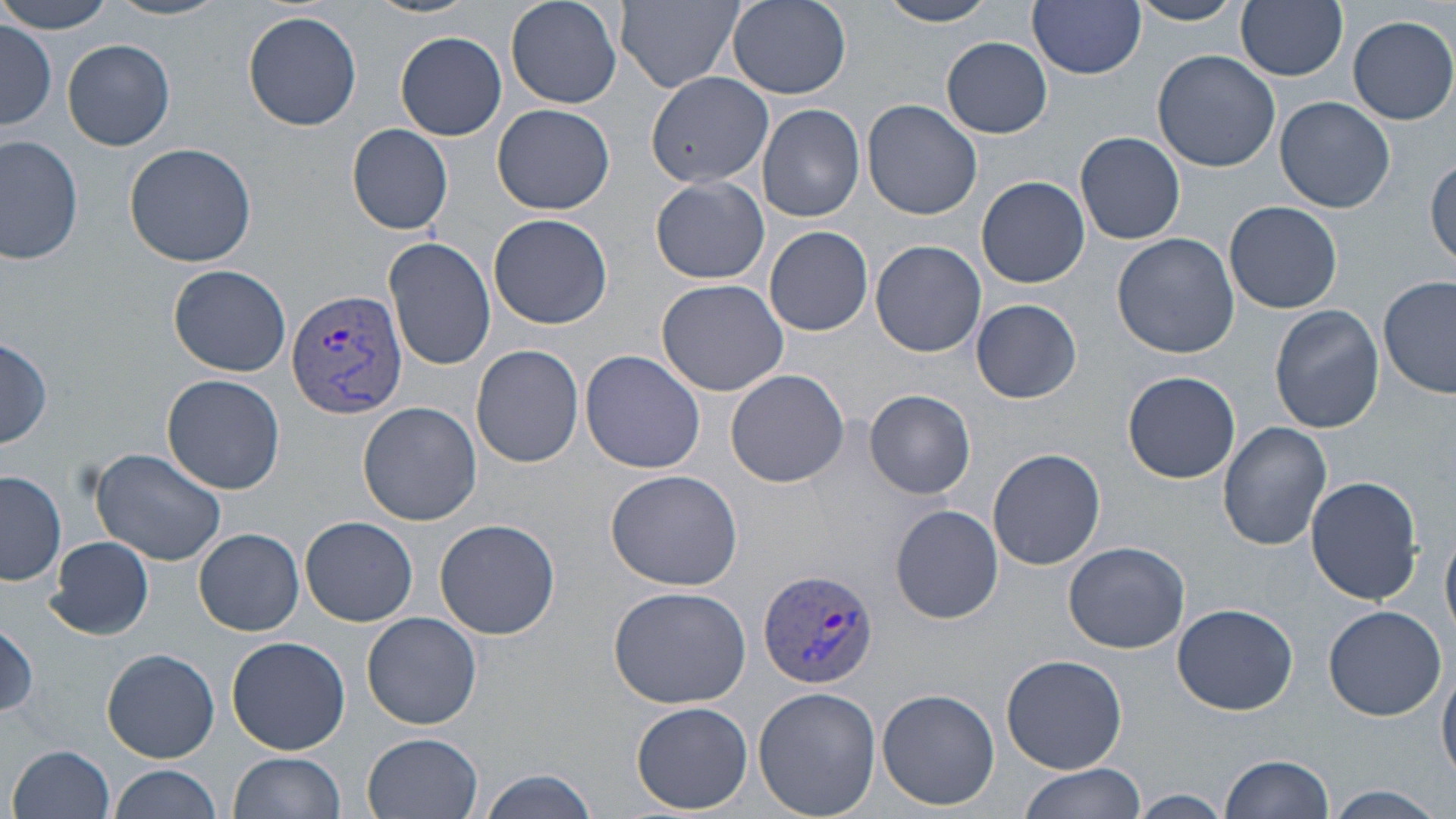

Approximate bounding boxes as named x1/y1/x2/y2 corners in pixels. Uninfected red blood cell locations: (x1=2, y1=0, x2=117, y2=34), (x1=107, y1=0, x2=231, y2=21), (x1=364, y1=0, x2=483, y2=19), (x1=506, y1=0, x2=623, y2=108), (x1=727, y1=0, x2=852, y2=98), (x1=878, y1=0, x2=999, y2=26), (x1=1129, y1=0, x2=1244, y2=25), (x1=1237, y1=0, x2=1348, y2=81), (x1=616, y1=1, x2=745, y2=93), (x1=1028, y1=1, x2=1145, y2=79), (x1=244, y1=11, x2=363, y2=131), (x1=1348, y1=14, x2=1456, y2=124), (x1=1, y1=24, x2=55, y2=130), (x1=395, y1=31, x2=506, y2=141), (x1=941, y1=38, x2=1052, y2=138), (x1=63, y1=39, x2=175, y2=151), (x1=1151, y1=48, x2=1279, y2=174), (x1=644, y1=70, x2=773, y2=191), (x1=1275, y1=96, x2=1397, y2=214), (x1=863, y1=101, x2=983, y2=220), (x1=492, y1=103, x2=615, y2=215), (x1=757, y1=104, x2=865, y2=222), (x1=345, y1=124, x2=455, y2=235), (x1=1074, y1=132, x2=1185, y2=245), (x1=1, y1=135, x2=84, y2=266), (x1=124, y1=141, x2=259, y2=267), (x1=1428, y1=154, x2=1456, y2=266), (x1=976, y1=175, x2=1090, y2=288), (x1=651, y1=176, x2=768, y2=284), (x1=1224, y1=200, x2=1342, y2=313), (x1=489, y1=213, x2=614, y2=330), (x1=765, y1=225, x2=873, y2=336), (x1=1111, y1=231, x2=1240, y2=357), (x1=383, y1=236, x2=496, y2=370), (x1=870, y1=240, x2=986, y2=357), (x1=169, y1=264, x2=293, y2=376), (x1=1379, y1=275, x2=1456, y2=401), (x1=655, y1=277, x2=789, y2=396), (x1=971, y1=298, x2=1083, y2=404), (x1=1268, y1=305, x2=1385, y2=433), (x1=1, y1=337, x2=53, y2=452), (x1=471, y1=344, x2=584, y2=467), (x1=581, y1=349, x2=705, y2=474), (x1=725, y1=369, x2=849, y2=488), (x1=1123, y1=370, x2=1241, y2=484), (x1=162, y1=375, x2=286, y2=494), (x1=864, y1=389, x2=976, y2=499), (x1=358, y1=401, x2=481, y2=526), (x1=1217, y1=422, x2=1333, y2=550), (x1=90, y1=445, x2=226, y2=567), (x1=987, y1=448, x2=1106, y2=571), (x1=605, y1=468, x2=743, y2=592), (x1=1, y1=470, x2=66, y2=587), (x1=1305, y1=475, x2=1424, y2=607), (x1=889, y1=504, x2=1004, y2=625), (x1=301, y1=515, x2=418, y2=626), (x1=435, y1=519, x2=558, y2=641), (x1=1443, y1=520, x2=1456, y2=640), (x1=194, y1=528, x2=303, y2=635), (x1=45, y1=536, x2=154, y2=641), (x1=1062, y1=540, x2=1190, y2=654), (x1=606, y1=586, x2=752, y2=709), (x1=1170, y1=604, x2=1298, y2=714), (x1=1322, y1=605, x2=1448, y2=720), (x1=362, y1=612, x2=482, y2=730), (x1=0, y1=623, x2=39, y2=723), (x1=226, y1=636, x2=350, y2=755), (x1=102, y1=648, x2=220, y2=762), (x1=1002, y1=653, x2=1128, y2=774), (x1=1438, y1=661, x2=1456, y2=783), (x1=753, y1=686, x2=881, y2=819), (x1=876, y1=688, x2=1000, y2=810), (x1=632, y1=702, x2=752, y2=815), (x1=363, y1=732, x2=483, y2=818), (x1=9, y1=744, x2=117, y2=819), (x1=229, y1=752, x2=346, y2=819), (x1=1220, y1=753, x2=1333, y2=819), (x1=1018, y1=763, x2=1142, y2=819), (x1=109, y1=764, x2=220, y2=819), (x1=475, y1=771, x2=598, y2=818), (x1=1320, y1=785, x2=1448, y2=818), (x1=1128, y1=790, x2=1232, y2=817). Plasmodium vivax-infected red blood cell locations: (x1=287, y1=285, x2=407, y2=421), (x1=758, y1=569, x2=879, y2=687). Slide-level diagnosis: Plasmodium vivax. Image is 1456×819 pixels. Single field of view. Captured at 1000x magnification. Thin blood film. May-Grünwald-Giemsa stain. Light microscopy.